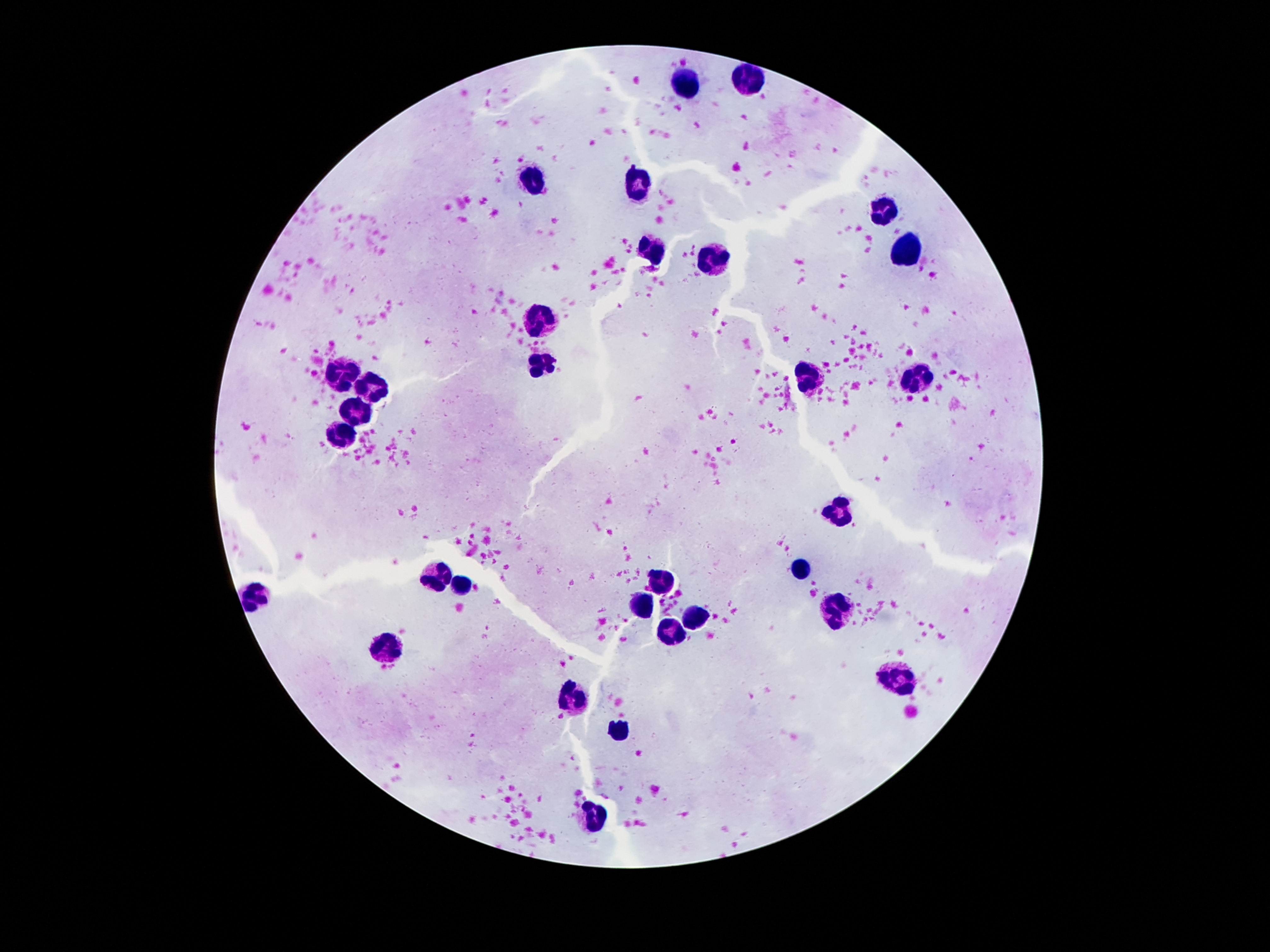

Approximate centers as {x, y} in pixels.
Summary:
  - Leukocyte locations: {742, 81}, {685, 85}, {638, 179}, {531, 181}, {882, 211}, {651, 247}, {905, 250}, {708, 258}, {542, 319}, {544, 358}, {350, 369}, {916, 379}, {812, 383}, {376, 387}, {358, 413}, {343, 431}, {839, 511}, {801, 570}, {435, 578}, {662, 581}, {458, 587}, {256, 596}, {644, 605}, {835, 612}, {694, 614}, {672, 632}, {388, 646}, {899, 680}, {572, 704}, {621, 732}, {594, 813}
  - Patient malaria status: negative
  - Preparation: thick blood film
  - Capture: smartphone camera through the microscope eyepiece
  - Stain: Giemsa
  - Image size: 1270×952 pixels
  - Field of view: one from this slide
  - Magnification: 100x